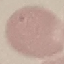
Malaria status: uninfected. Thin smear of blood. Automatically extracted cell patch, resized to 64 × 64 pixels. Acquired by smartphone through the microscope eyepiece. Giemsa stain.